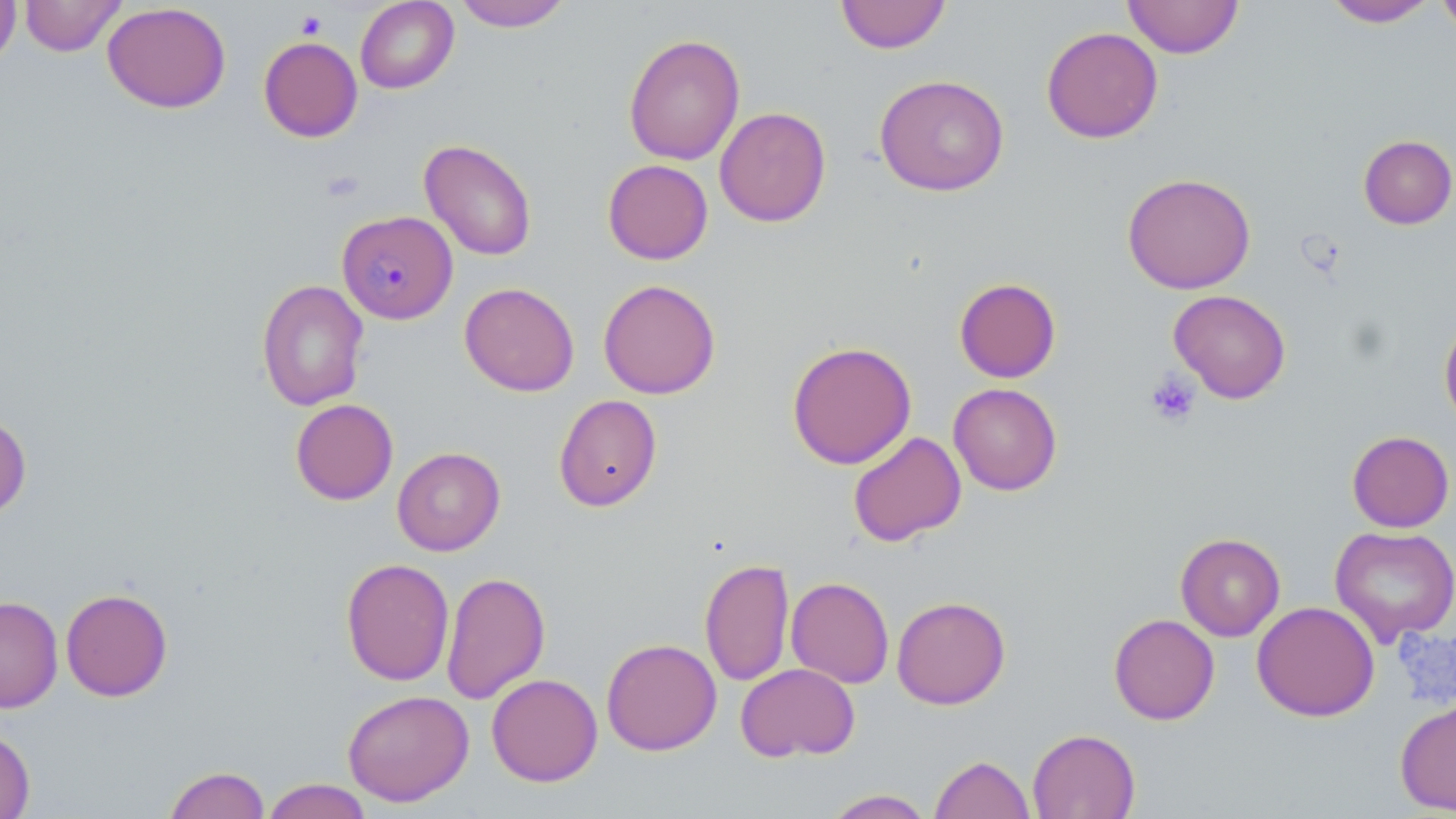

Plasmodium malariae-infected red blood cell locations = approximate bounding boxes as (x1, y1, x2, y2) in pixels: (336, 210, 457, 324)
slide-level diagnosis = Plasmodium malariae
modality = light microscopy
uninfected red blood cell locations = approximate bounding boxes as (x1, y1, x2, y2) in pixels: (0, 0, 21, 70), (18, 0, 127, 57), (355, 0, 459, 94), (453, 0, 573, 31), (834, 0, 952, 54), (1123, 0, 1244, 58), (1323, 0, 1438, 27), (1436, 0, 1456, 38), (102, 2, 231, 114), (1041, 26, 1163, 143), (623, 33, 745, 166), (258, 36, 362, 142), (874, 74, 1010, 196), (714, 106, 832, 227), (1358, 134, 1456, 229), (419, 139, 537, 261), (603, 159, 713, 265), (1122, 172, 1256, 295), (954, 277, 1061, 382), (256, 279, 369, 412), (598, 279, 721, 399), (459, 282, 579, 396), (1168, 289, 1292, 404), (1439, 316, 1456, 430), (786, 340, 917, 469), (948, 382, 1062, 495), (553, 394, 662, 512), (290, 398, 398, 505), (0, 411, 32, 521), (1346, 430, 1454, 532), (848, 431, 966, 547), (392, 447, 505, 556), (1330, 526, 1456, 645), (1175, 533, 1286, 641), (699, 557, 795, 686), (341, 558, 454, 686), (441, 571, 551, 706), (786, 576, 894, 688), (60, 588, 173, 701), (0, 595, 63, 713), (891, 595, 1011, 709), (1252, 601, 1380, 722), (1108, 613, 1220, 725), (601, 638, 722, 756), (736, 663, 860, 762), (486, 673, 603, 787), (342, 689, 474, 806), (1395, 698, 1456, 816), (0, 728, 35, 818), (1027, 728, 1140, 819), (930, 754, 1035, 819), (163, 766, 270, 818), (261, 779, 373, 819), (822, 788, 935, 818)
stain = May-Grünwald-Giemsa
magnification = 1000x
image size = 1456×819 pixels
preparation = thin blood film
platelet locations = approximate bounding boxes as (x1, y1, x2, y2) in pixels: (295, 10, 327, 39), (1145, 372, 1201, 427)
field of view = one of a larger specimen